State the blood parasite species.
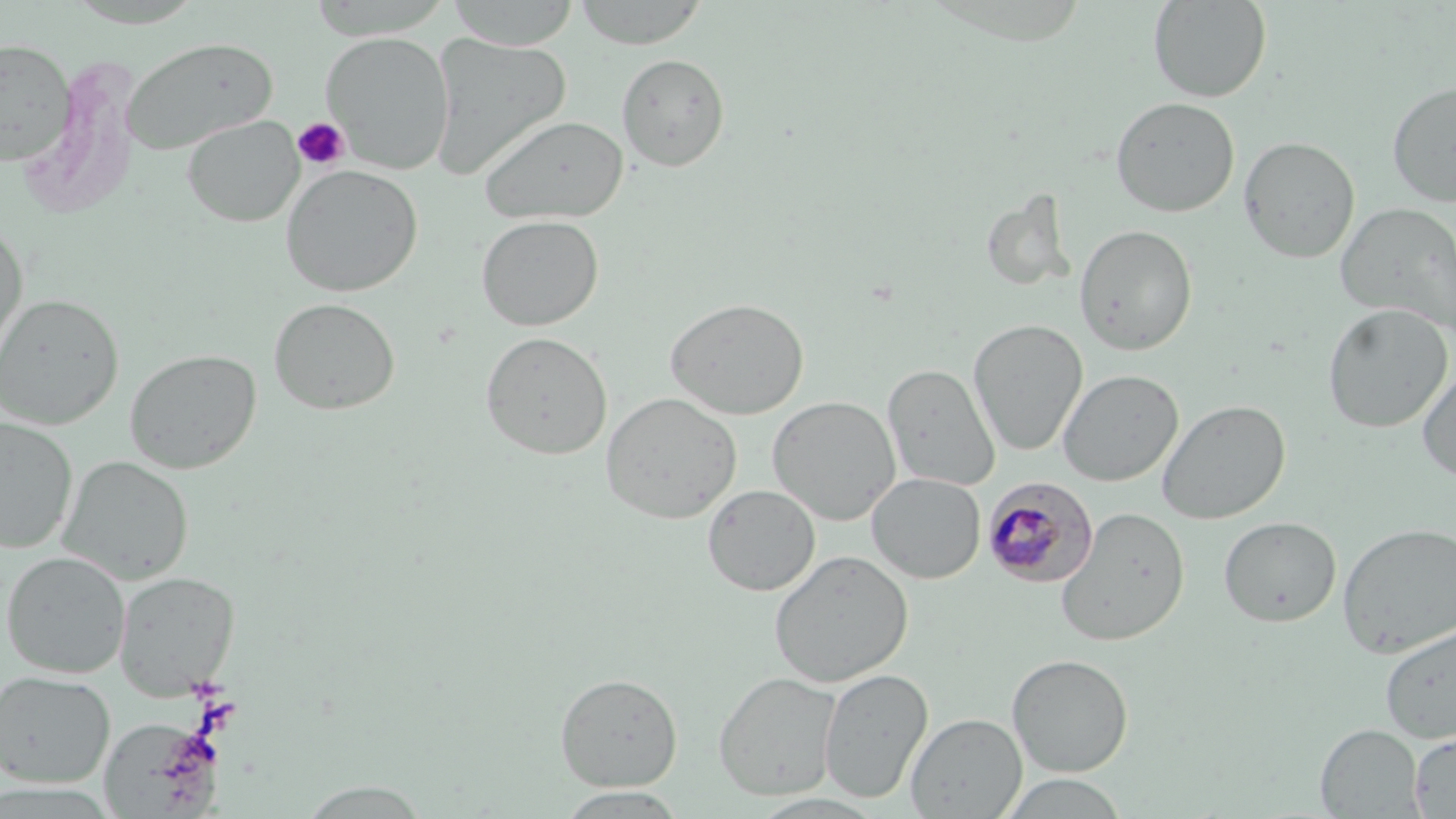

Plasmodium malariae.

Summary:
  - Coordinate format: approximate bounding boxes as (x1,y1)-(x2,y2) corner pairs in pixels
  - Uninfected red blood cell locations: (446,0)-(581,50), (571,0)-(710,49), (1148,0)-(1272,103), (320,31)-(455,173), (429,33)-(572,179), (121,36)-(278,155), (0,39)-(76,168), (616,53)-(730,171), (1386,79)-(1456,208), (1110,97)-(1240,218), (182,115)-(304,227), (479,115)-(629,223), (1238,136)-(1360,264), (280,163)-(424,297), (980,191)-(1077,293), (1336,201)-(1456,336), (476,214)-(604,331), (0,223)-(29,365), (1075,224)-(1198,356), (0,293)-(123,430), (268,297)-(400,415), (665,297)-(809,419), (1322,303)-(1453,433), (968,319)-(1088,456), (480,331)-(613,460), (124,348)-(262,474), (1416,362)-(1456,483), (882,363)-(1000,490), (1058,368)-(1183,487), (600,392)-(742,524), (767,396)-(901,525), (1157,399)-(1290,525), (0,417)-(77,554), (57,455)-(194,585), (867,473)-(986,583), (702,484)-(820,596), (1055,507)-(1191,647), (1218,516)-(1341,627), (1337,521)-(1456,658), (769,550)-(913,687), (1,551)-(131,678), (113,570)-(240,699), (1379,622)-(1456,744), (1007,653)-(1134,777), (818,667)-(933,804), (0,670)-(115,788), (714,672)-(842,800), (555,673)-(682,791), (906,712)-(1027,818), (1315,724)-(1424,817), (1409,732)-(1456,817), (999,773)-(1129,818), (295,781)-(433,818), (555,788)-(689,818), (748,793)-(887,818)
  - Platelet locations: (292,117)-(350,172)
  - Plasmodium malariae-infected red blood cell locations: (982,476)-(1098,588)
  - Image size: 1456×819 pixels
  - Preparation: thin blood film
  - Modality: light microscopy
  - Magnification: 1000x
  - Field of view: single
  - Stain: May-Grünwald-Giemsa